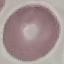

Summary:
  - Result: negative for malaria parasites
  - Preparation: thin blood smear
  - Capture: smartphone camera at the microscope eyepiece
  - Stain: Giemsa
  - Image type: automatically extracted cell patch, resized to 64 × 64 pixels